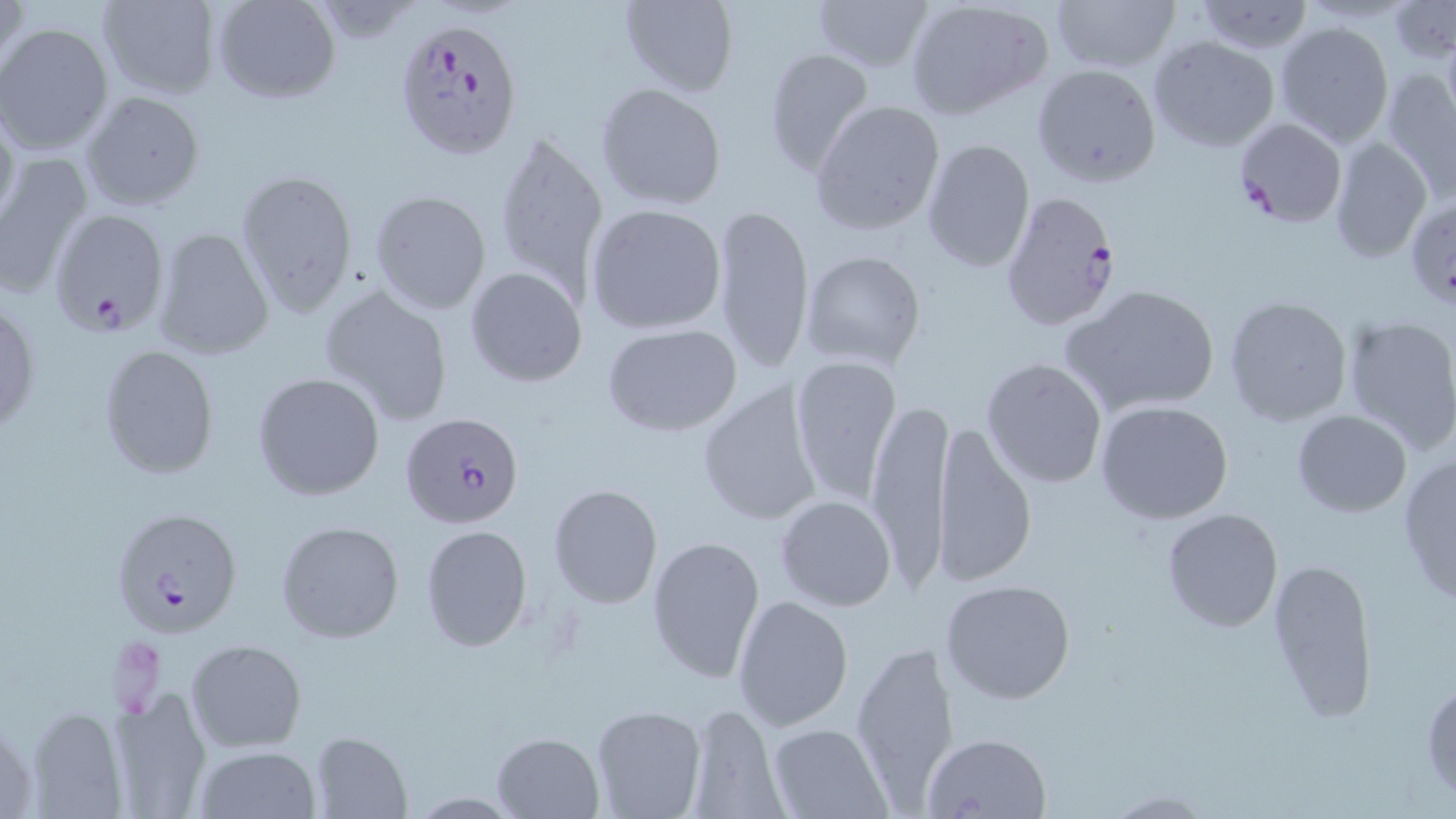
Summary:
  - Coordinate format: approximate bounding boxes as (x1,y1)-(x2,y2) corner pairs in pixels
  - Uninfected red blood cell locations: (1,0)-(30,91), (97,0)-(222,99), (212,0)-(340,103), (619,0)-(739,97), (810,0)-(933,73), (905,0)-(1053,122), (1052,0)-(1180,74), (1193,0)-(1316,54), (1388,0)-(1456,62), (1273,20)-(1395,150), (1,23)-(117,156), (1149,37)-(1280,152), (761,47)-(875,177), (1032,63)-(1162,188), (1380,67)-(1456,198), (595,82)-(729,210), (79,90)-(205,213), (809,98)-(946,236), (0,103)-(20,234), (490,125)-(610,298), (1327,137)-(1432,262), (921,138)-(1034,271), (0,150)-(94,301), (234,167)-(359,318), (369,190)-(492,315), (1406,193)-(1454,308), (585,202)-(727,335), (710,204)-(817,374), (151,227)-(274,361), (799,249)-(927,369), (465,266)-(587,387), (1063,282)-(1221,416), (318,284)-(456,430), (1224,295)-(1354,428), (1,298)-(39,436), (1341,314)-(1456,452), (603,323)-(744,438), (98,345)-(221,479), (789,355)-(904,510), (980,357)-(1107,489), (251,371)-(385,501), (696,381)-(824,526), (868,395)-(951,585), (1094,399)-(1235,523), (1291,410)-(1412,517), (933,422)-(1037,587), (1397,456)-(1456,605), (548,483)-(664,609), (775,494)-(896,611), (1160,508)-(1283,632), (278,520)-(403,644), (419,524)-(533,652), (646,533)-(766,684), (1267,557)-(1377,722), (941,577)-(1075,704), (733,593)-(854,731), (185,637)-(307,752), (848,637)-(962,805), (1422,680)-(1455,801), (108,691)-(214,816), (686,703)-(785,819), (589,704)-(709,819), (23,705)-(133,818), (766,723)-(891,819), (311,731)-(412,818), (491,731)-(604,816), (922,732)-(1055,818), (190,744)-(322,819), (1103,790)-(1213,817)
  - Plasmodium falciparum-infected red blood cell locations: (396,17)-(525,161), (1232,117)-(1348,228), (998,189)-(1120,334), (49,208)-(170,337), (402,412)-(525,528), (109,504)-(244,638)
  - Slide-level diagnosis: Plasmodium falciparum
  - Image size: 1456×819 pixels
  - Magnification: 1000x
  - Field of view: one of a larger specimen
  - Modality: optical microscopy
  - Stain: May-Grünwald-Giemsa
  - Preparation: thin blood film